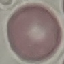

Malaria status: uninfected. Giemsa stain. Thin smear of blood. Automatically extracted cell patch, resized to 64 × 64 pixels. Photographed with a smartphone camera at the microscope eyepiece.